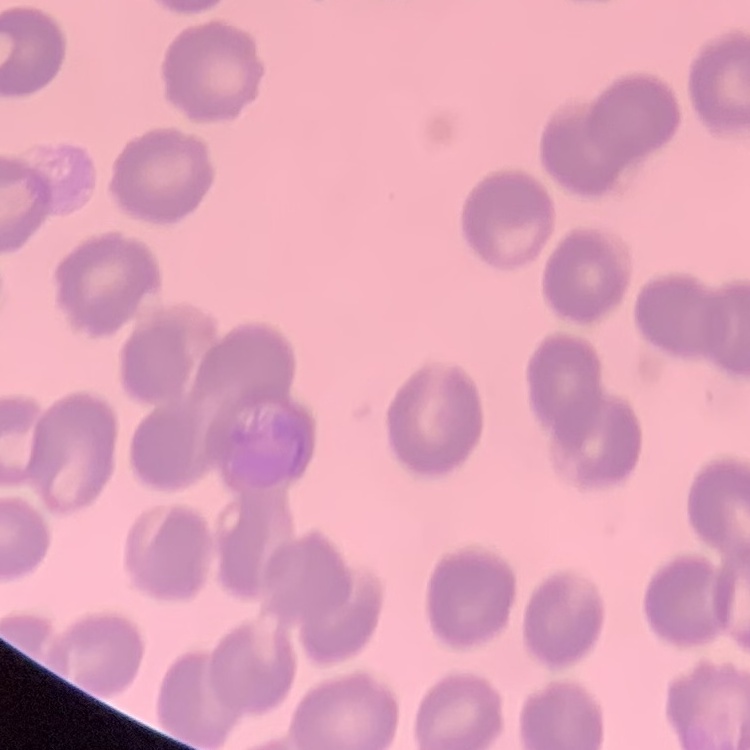

{
  "red_blood_cell_morphology": "no rouleaux formation",
  "image_type": "one tile cut from a larger photomicrograph",
  "preparation": "thin blood smear",
  "stain": "Field's or Giemsa"
}